Report the malaria status of this cell.
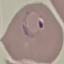

Parasitized.

{
  "capture": "smartphone camera at the microscope eyepiece",
  "preparation": "thin smear",
  "image_type": "cell patch, automatically extracted from a larger field of view and resized to 64 × 64 pixels",
  "stain": "Giemsa"
}